Identify the cell.
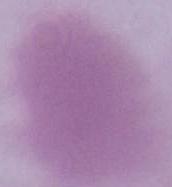
An erythrocyte.

1000x magnification. Photomicrograph.